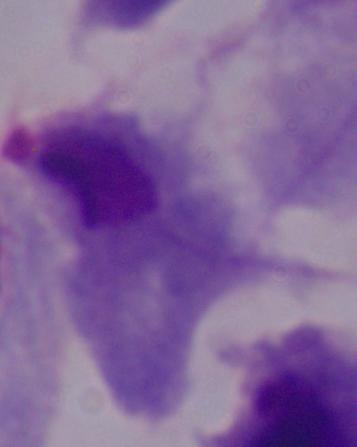

A trichomonad is shown. Photomicrograph. 1000x magnification.